Point out each Plasmodium parasite.
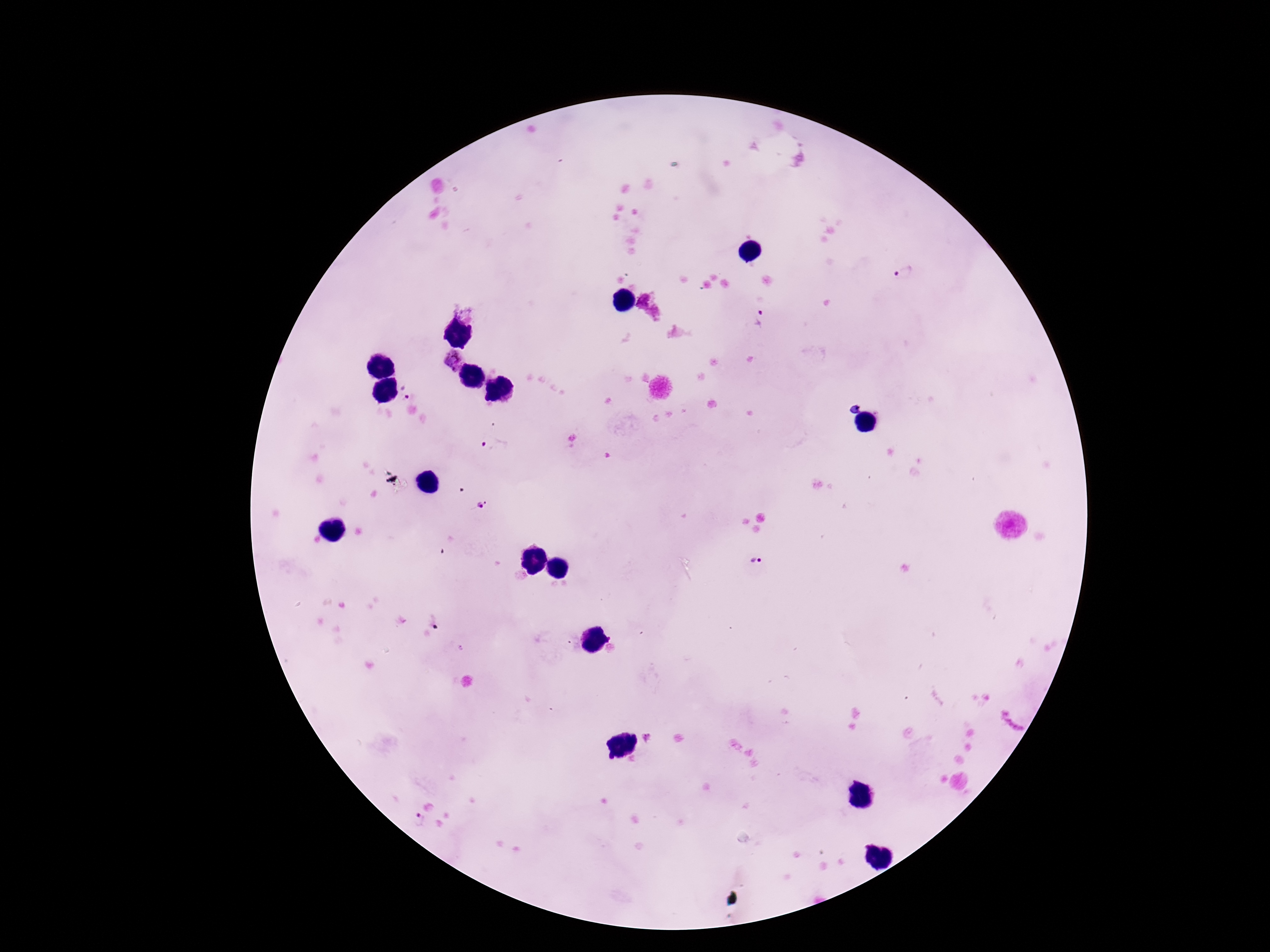

Approximate centers as {x, y} in pixels.
Plasmodium parasites: {905, 272}, {760, 318}, {453, 359}, {407, 389}, {494, 449}, {483, 505}, {756, 560}, {436, 619}, {649, 736}, {418, 818}.

Summary:
  - Magnification: 100x
  - Patient malaria status: positive
  - Capture: smartphone camera through the microscope eyepiece
  - Field of view: one from this slide
  - Image size: 1270×952 pixels
  - Preparation: thick peripheral-blood smear
  - Stain: Giemsa